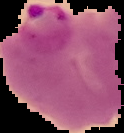
image type = segmented cell region on a black background
image size = 124×133 pixels
result = Plasmodium parasites detected
preparation = thin blood film